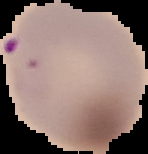

malaria status = parasitized
image type = segmented cell region with the area outside set to black
image size = 148×154 pixels
preparation = thin blood film